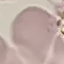

result: no malaria parasites detected
image_type: automatically extracted cell patch, resized to 64 × 64 pixels
stain: Giemsa
preparation: thin smear
capture: smartphone through the microscope eyepiece